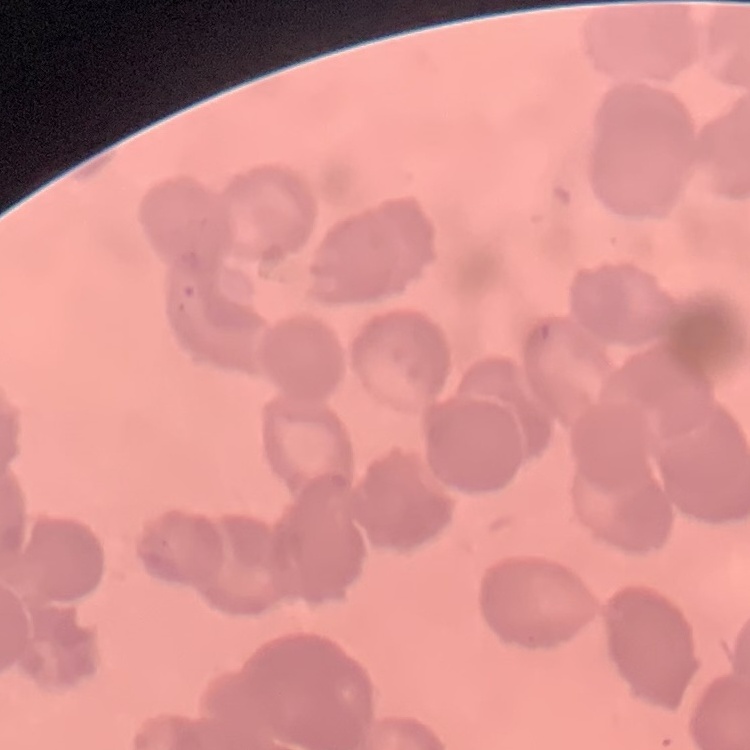

The erythrocytes exhibit rouleaux formation. Stained with either Field's or Giemsa. Thin blood smear. Square crop of a larger photomicrograph.